Assess the morphology of the erythrocytes.
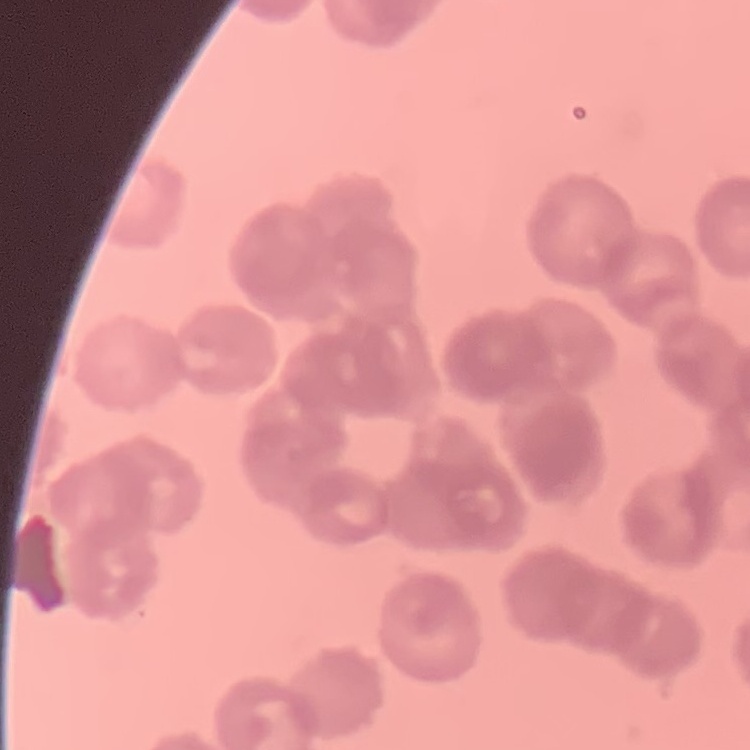

Rouleaux formation.

Summary:
  - Stain: Field's or Giemsa
  - Preparation: thin peripheral smear
  - Image type: one tile cut from a larger photomicrograph